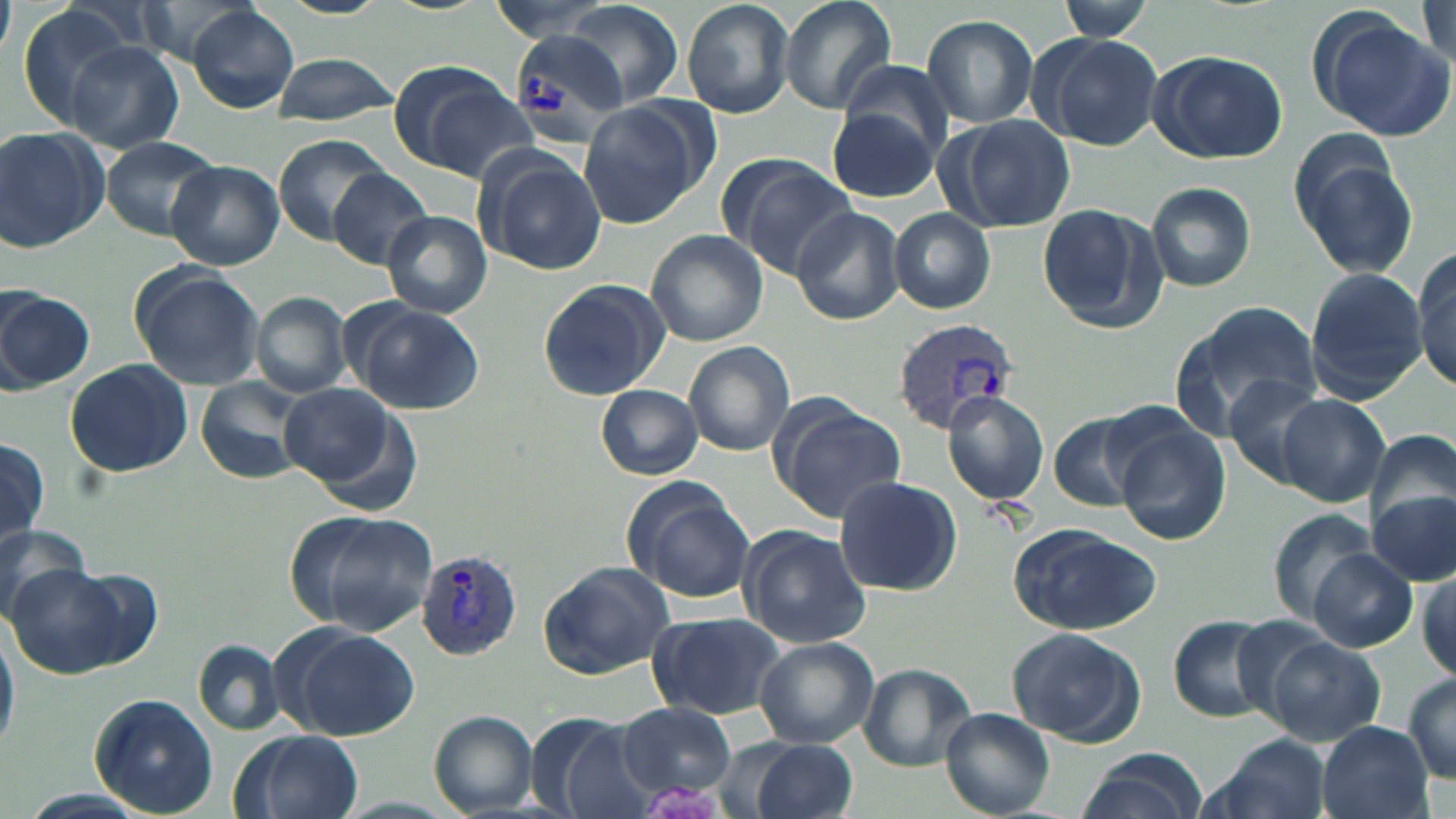
slide-level diagnosis = Plasmodium vivax
image size = 1456×819 pixels
magnification = 1000x
platelet locations = approximate bounding boxes as [x1, y1, x2, y2] in pixels: [641, 778, 721, 819]
uninfected red blood cell locations = approximate bounding boxes as [x1, y1, x2, y2] in pixels: [681, 0, 796, 119], [776, 0, 898, 115], [1054, 0, 1154, 41], [560, 2, 683, 112], [187, 4, 298, 112], [1418, 4, 1454, 69], [15, 5, 144, 129], [1307, 9, 1454, 141], [920, 14, 1039, 130], [1031, 32, 1166, 151], [65, 40, 184, 154], [1147, 48, 1288, 165], [270, 52, 399, 125], [385, 60, 531, 179], [579, 99, 713, 229], [825, 104, 940, 203], [939, 113, 1076, 232], [0, 127, 107, 251], [273, 133, 387, 245], [100, 136, 222, 240], [1286, 138, 1420, 282], [477, 150, 605, 275], [720, 155, 857, 280], [167, 161, 284, 270], [327, 168, 433, 270], [1146, 182, 1257, 293], [1034, 202, 1169, 336], [791, 207, 905, 326], [889, 208, 995, 313], [383, 210, 493, 317], [645, 229, 767, 347], [1411, 248, 1456, 391], [128, 263, 266, 390], [1303, 267, 1427, 402], [537, 278, 670, 399], [0, 287, 94, 392], [252, 293, 352, 397], [347, 300, 485, 416], [1173, 301, 1325, 439], [684, 340, 795, 456], [65, 359, 192, 478], [1222, 373, 1329, 488], [194, 379, 306, 488], [279, 382, 405, 496], [596, 384, 703, 480], [943, 390, 1049, 506], [1277, 393, 1390, 506], [773, 404, 905, 523], [1049, 414, 1151, 512], [1113, 420, 1230, 546], [1368, 426, 1456, 531], [0, 438, 49, 547], [834, 475, 962, 596], [624, 482, 755, 604], [1370, 490, 1455, 584], [1267, 507, 1378, 625], [289, 509, 440, 639], [0, 521, 98, 624], [1009, 523, 1164, 636], [738, 525, 872, 647], [1306, 548, 1418, 652], [536, 560, 678, 678], [3, 564, 143, 677], [1414, 570, 1454, 685], [648, 611, 785, 721], [1166, 614, 1277, 723], [0, 620, 19, 759], [281, 624, 419, 742], [1008, 626, 1145, 747], [1256, 630, 1387, 746], [752, 636, 878, 749], [195, 642, 284, 733], [860, 663, 976, 769], [1402, 672, 1456, 783], [88, 693, 219, 819], [617, 702, 737, 801], [939, 708, 1056, 818], [427, 710, 540, 817], [525, 713, 650, 819], [1317, 723, 1432, 819], [233, 730, 363, 819], [1202, 736, 1334, 819], [738, 738, 858, 819], [1078, 747, 1207, 819], [18, 789, 148, 819]
Plasmodium vivax-infected red blood cell locations = approximate bounding boxes as [x1, y1, x2, y2] in pixels: [509, 28, 629, 144], [891, 319, 1019, 436], [416, 549, 524, 659]
preparation = thin blood film
field of view = single
stain = May-Grünwald-Giemsa
modality = optical microscopy